Assess this cell for malaria.
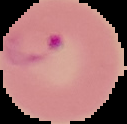
It is parasitized.

Segmented cell region on a black background. Image is 127×124 pixels. From a thin blood film.